Assess for Plasmodium parasites.
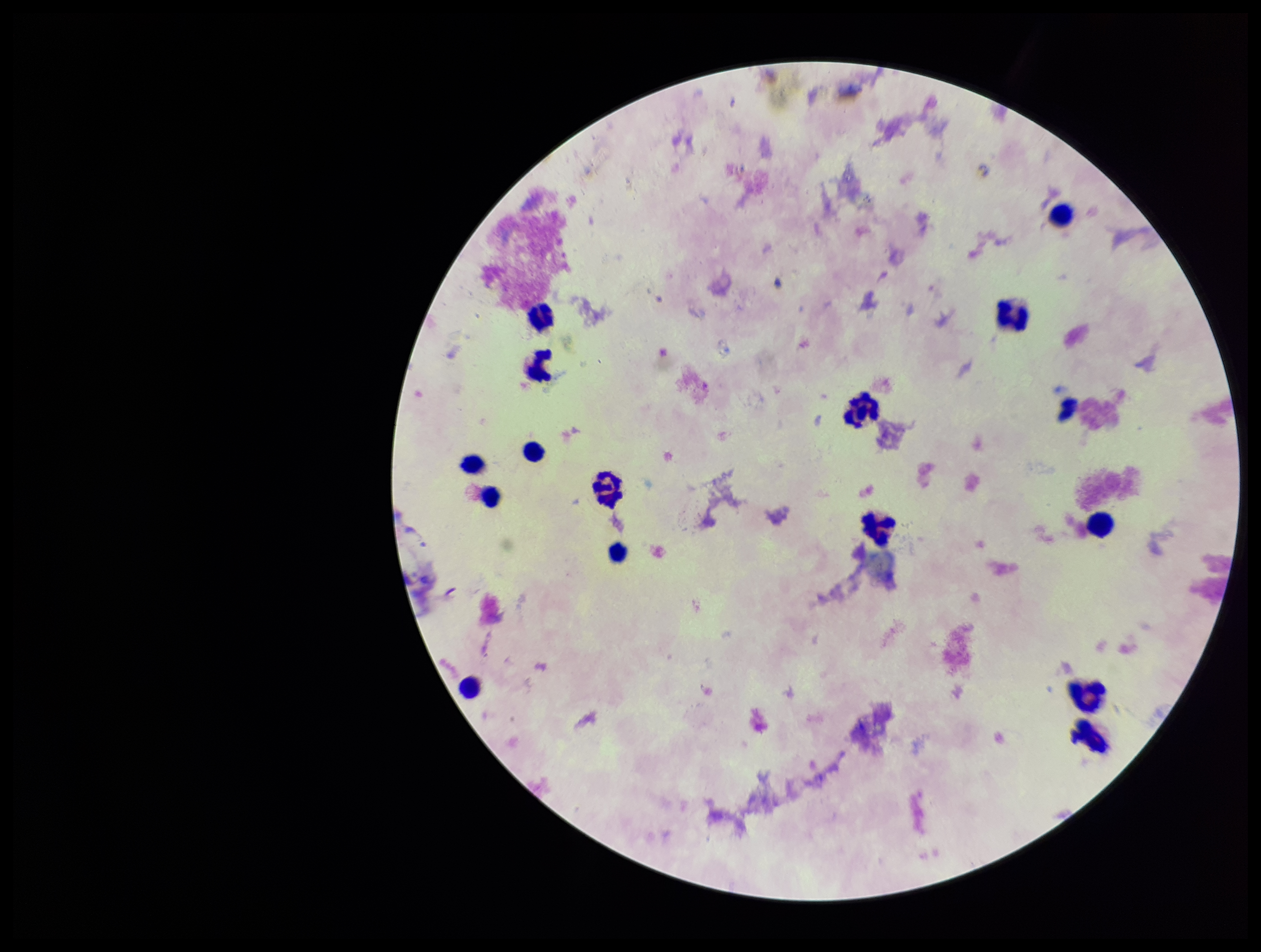
None seen.

field of view = one from this slide
leukocyte count = 15
stain = Giemsa
capture = smartphone photograph through the microscope eyepiece
parasite count = 0
preparation = thick smear
patient malaria status = negative
image size = 1261×952 pixels